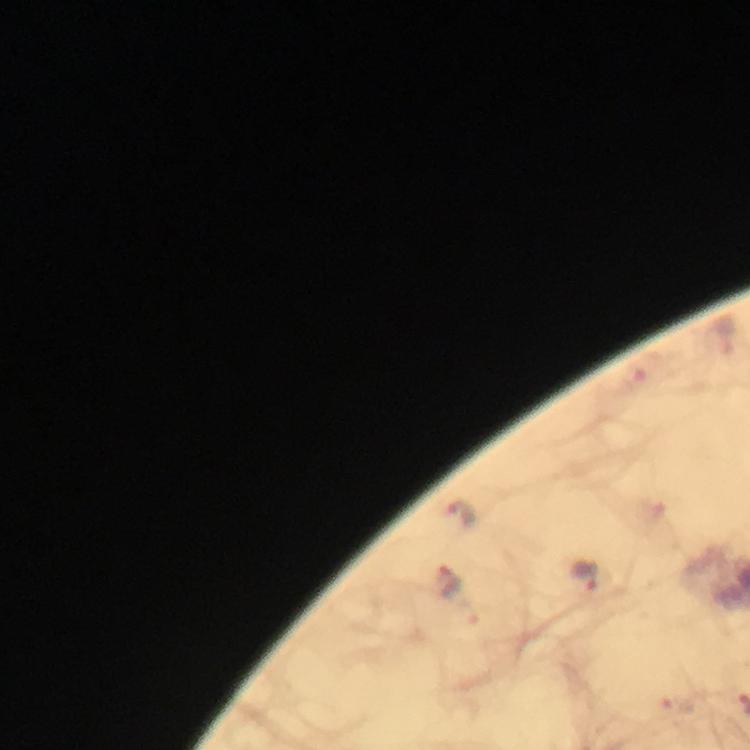

Approximate centers as {x, y} in pixels.
Summary:
  - Plasmodium parasite locations: {727, 339}, {633, 379}, {657, 500}, {463, 515}, {587, 579}, {448, 584}, {678, 705}
  - Capture: smartphone mounted on the microscope
  - Immersion oil: applied
  - Context: from a malaria diagnostic workup
  - Preparation: thick blood film
  - Image size: 750×750 pixels
  - Magnification: 100x
  - Cropped from: one field of view
  - Stain: Giemsa